Classify this cell by malaria status.
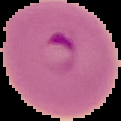

It is parasitized.

From a thin blood film. Segmented cell region on a black background. Image is 121×121 pixels.